Locate and identify every blood parasite.
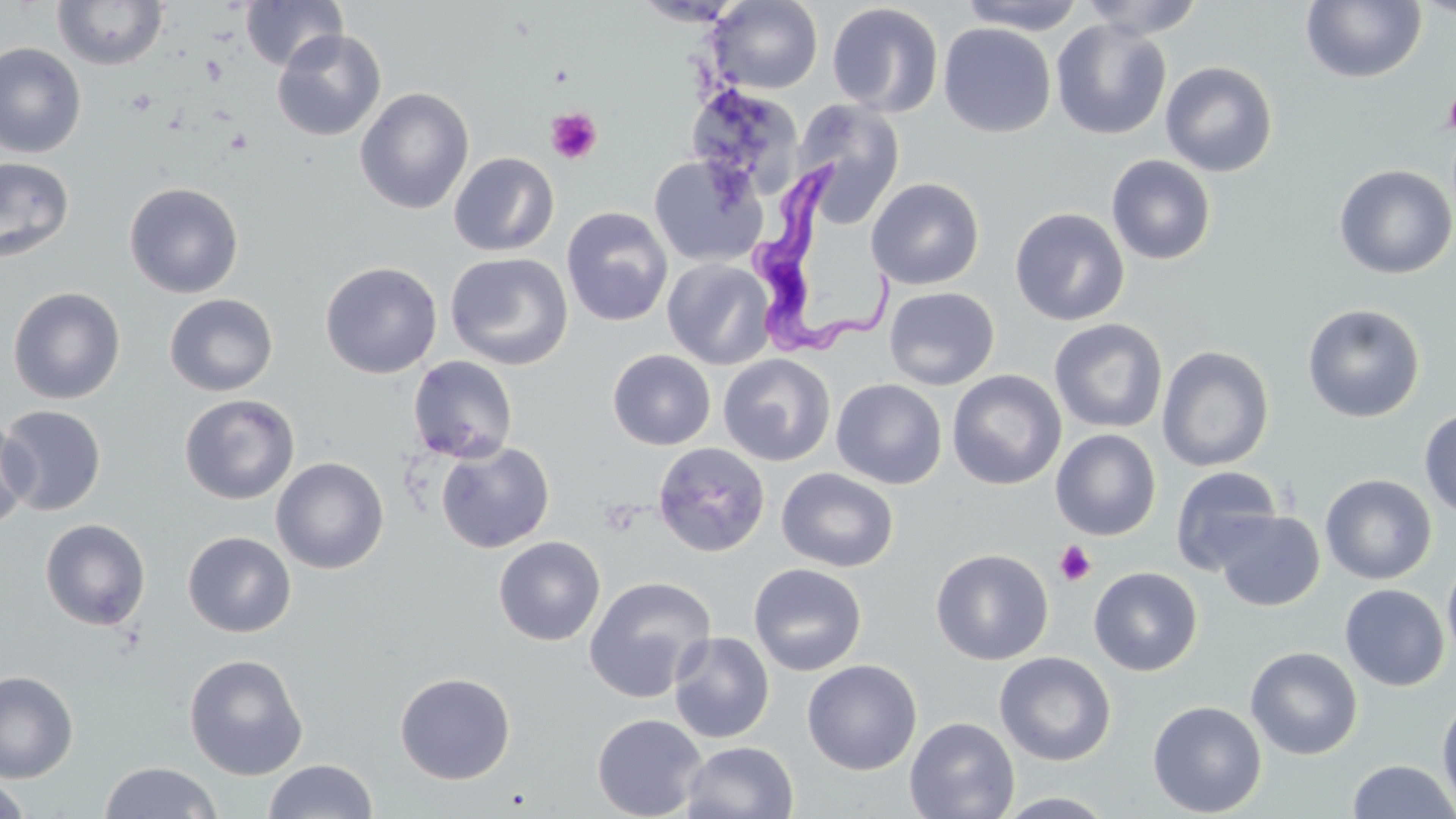
Approximate bounding boxes as named x1/y1/x2/y2 corners in pixels.
Trypanosoma brucei: (x1=751, y1=165, x2=896, y2=357).
No Plasmodium falciparum, Plasmodium ovale, Plasmodium malariae, Plasmodium vivax, or Babesia divergens observed.

Summary:
  - Uninfected red blood cell locations: (x1=239, y1=0, x2=348, y2=72), (x1=709, y1=0, x2=823, y2=93), (x1=954, y1=0, x2=1088, y2=34), (x1=1078, y1=0, x2=1205, y2=39), (x1=1412, y1=0, x2=1456, y2=20), (x1=52, y1=1, x2=170, y2=70), (x1=631, y1=1, x2=748, y2=27), (x1=1301, y1=1, x2=1426, y2=84), (x1=826, y1=3, x2=944, y2=117), (x1=1051, y1=19, x2=1172, y2=140), (x1=938, y1=23, x2=1056, y2=138), (x1=271, y1=28, x2=387, y2=142), (x1=0, y1=43, x2=86, y2=159), (x1=1160, y1=60, x2=1278, y2=177), (x1=355, y1=87, x2=474, y2=214), (x1=694, y1=90, x2=804, y2=203), (x1=793, y1=99, x2=907, y2=224), (x1=448, y1=152, x2=559, y2=257), (x1=649, y1=153, x2=766, y2=268), (x1=1106, y1=154, x2=1217, y2=266), (x1=0, y1=157, x2=75, y2=262), (x1=1334, y1=164, x2=1456, y2=279), (x1=866, y1=177, x2=984, y2=290), (x1=124, y1=181, x2=244, y2=298), (x1=561, y1=206, x2=673, y2=326), (x1=1009, y1=206, x2=1130, y2=326), (x1=445, y1=252, x2=573, y2=370), (x1=662, y1=258, x2=776, y2=370), (x1=320, y1=261, x2=442, y2=379), (x1=7, y1=286, x2=126, y2=404), (x1=884, y1=286, x2=1000, y2=390), (x1=164, y1=293, x2=279, y2=397), (x1=1301, y1=303, x2=1426, y2=423), (x1=1049, y1=317, x2=1168, y2=434), (x1=1157, y1=345, x2=1274, y2=472), (x1=606, y1=349, x2=716, y2=450), (x1=718, y1=353, x2=835, y2=467), (x1=407, y1=355, x2=519, y2=464), (x1=947, y1=370, x2=1066, y2=490), (x1=831, y1=379, x2=947, y2=489), (x1=179, y1=393, x2=300, y2=504), (x1=0, y1=404, x2=107, y2=516), (x1=1419, y1=408, x2=1456, y2=519), (x1=0, y1=416, x2=35, y2=531), (x1=1050, y1=429, x2=1162, y2=540), (x1=436, y1=440, x2=555, y2=553), (x1=651, y1=441, x2=771, y2=558), (x1=271, y1=456, x2=390, y2=574), (x1=1169, y1=465, x2=1283, y2=575), (x1=776, y1=467, x2=899, y2=573), (x1=1320, y1=474, x2=1437, y2=584), (x1=1214, y1=509, x2=1324, y2=611), (x1=40, y1=518, x2=151, y2=630), (x1=182, y1=531, x2=296, y2=637), (x1=493, y1=535, x2=606, y2=646), (x1=930, y1=548, x2=1054, y2=666), (x1=1442, y1=557, x2=1456, y2=667), (x1=748, y1=563, x2=868, y2=676), (x1=1089, y1=566, x2=1202, y2=676), (x1=583, y1=575, x2=717, y2=703), (x1=1339, y1=584, x2=1449, y2=691), (x1=668, y1=632, x2=775, y2=743), (x1=1245, y1=646, x2=1363, y2=759), (x1=994, y1=651, x2=1116, y2=766), (x1=184, y1=653, x2=308, y2=780), (x1=801, y1=659, x2=922, y2=775), (x1=0, y1=670, x2=78, y2=783), (x1=394, y1=671, x2=516, y2=784), (x1=1436, y1=695, x2=1456, y2=815), (x1=1148, y1=699, x2=1266, y2=817), (x1=591, y1=713, x2=707, y2=819), (x1=904, y1=716, x2=1019, y2=819), (x1=681, y1=740, x2=799, y2=819), (x1=262, y1=759, x2=377, y2=818), (x1=1346, y1=759, x2=1456, y2=818), (x1=98, y1=761, x2=223, y2=819), (x1=0, y1=775, x2=34, y2=819), (x1=994, y1=791, x2=1119, y2=818)
  - Platelet locations: (x1=1443, y1=86, x2=1456, y2=139), (x1=545, y1=107, x2=603, y2=165), (x1=1054, y1=541, x2=1096, y2=586)
  - Slide-level diagnosis: Trypanosoma brucei
  - Preparation: thin blood smear
  - Modality: light microscopy
  - Stain: May-Grünwald-Giemsa
  - Field of view: one of a larger specimen
  - Magnification: 1000x
  - Image size: 1456×819 pixels